Give the preparation type.
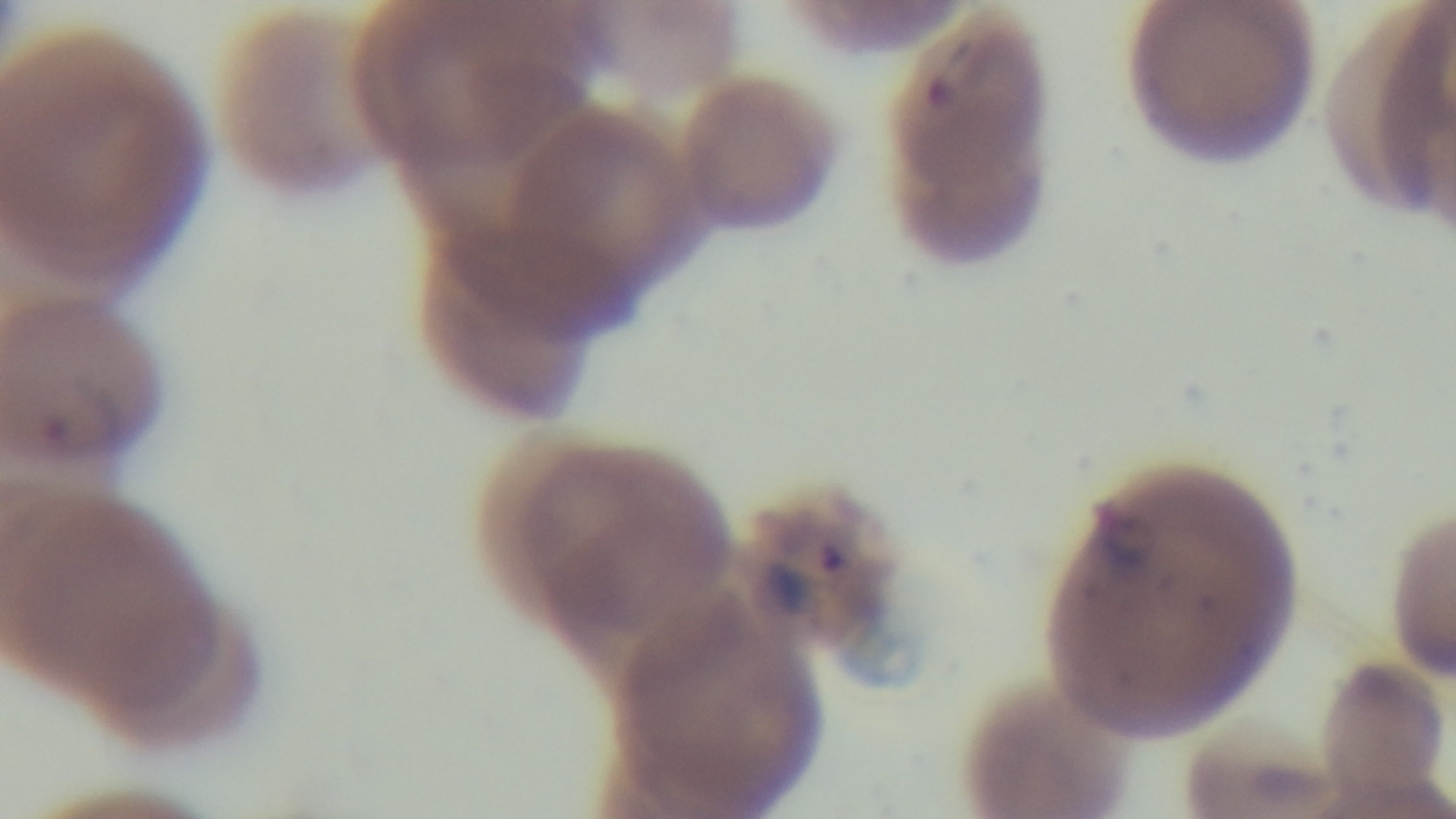
A thin smear.

Summary:
  - Stain: Giemsa
  - Field of view: one from the slide
  - Capture: mounted 4K digital camera
  - Objective: 100x oil immersion
  - Malaria status: positive
  - Modality: light microscopy